Comment on the morphology of the red blood cells.
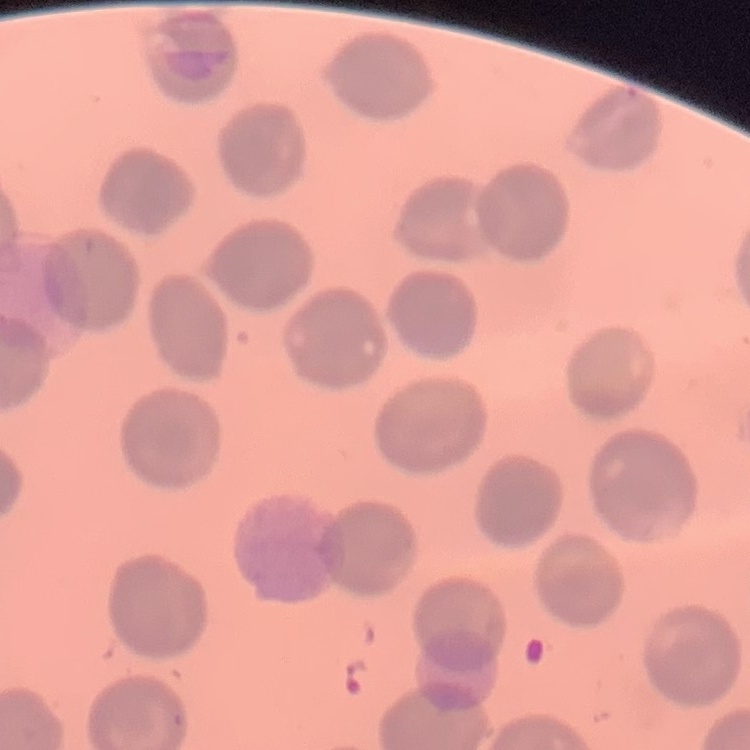

No rouleaux formation.

One tile cut from a larger photomicrograph. Thin blood film. Field's or Giemsa stain.